Mark where leukocytes are.
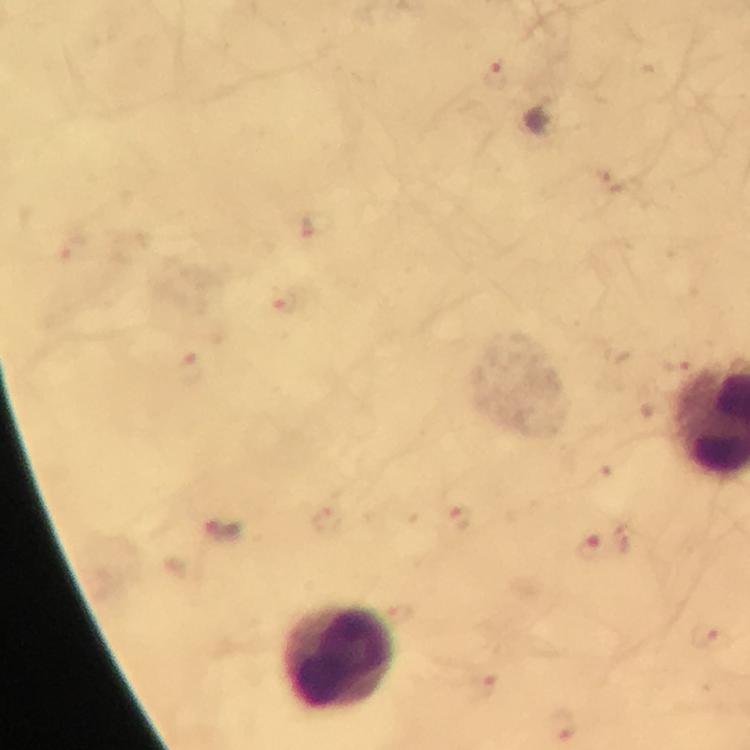

Approximate object centers, in pixels from the top-left corner.
Leukocytes: (x=342, y=659).

context: from a malaria diagnostic workup
cropped_from: a single field of view
capture: smartphone camera through the microscope
stain: Giemsa
magnification: 100x
image_size: 750×750 pixels
preparation: thick blood film
immersion_oil: used
malaria_parasite_locations: 'approximate object centers, in pixels from the top-left corner: (x=495, y=73), (x=319, y=225), (x=284, y=299), (x=189, y=367), (x=460, y=520), (x=222, y=530), (x=592, y=547), (x=706, y=635), (x=485, y=685), (x=562, y=723)'